Point out each Plasmodium parasite.
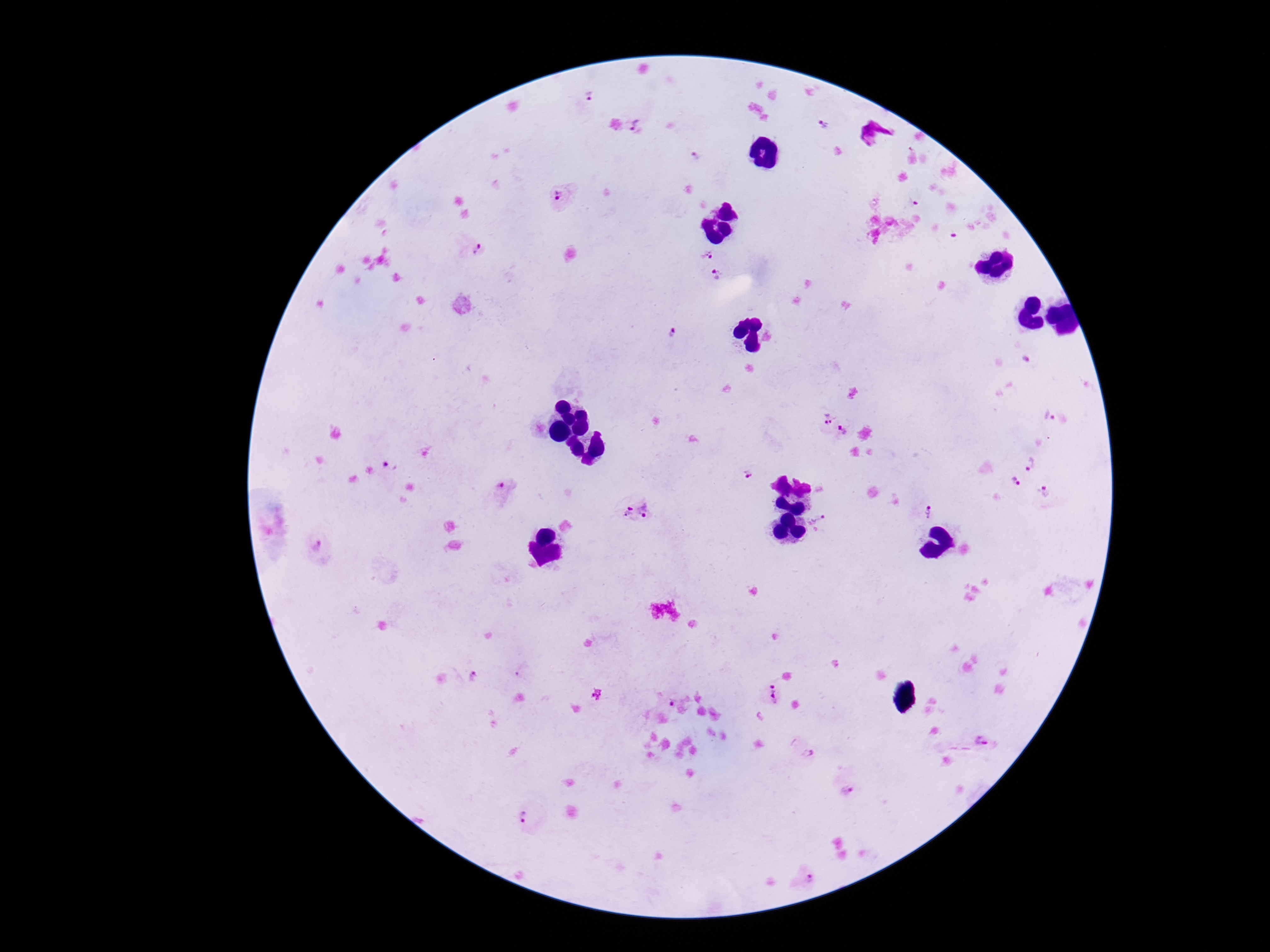
Approximate centers as [x, y] in pixels.
Plasmodium parasites: [587, 95], [825, 127], [642, 128], [695, 156], [558, 196], [914, 201], [954, 235], [472, 248], [704, 252], [719, 275], [675, 332], [1025, 360], [822, 417], [843, 433], [1030, 463], [389, 465], [743, 472], [1010, 490], [506, 492], [1043, 496], [622, 509], [928, 511], [648, 512], [821, 523], [318, 549], [475, 679], [597, 694], [774, 695], [672, 700], [979, 741], [804, 753], [846, 791], [527, 817], [805, 875].

Summary:
  - Field of view: single
  - Patient malaria status: infected
  - Capture: smartphone camera through the microscope eyepiece
  - Stain: Giemsa
  - Magnification: 100x
  - Image size: 1270×952 pixels
  - Preparation: thick blood smear